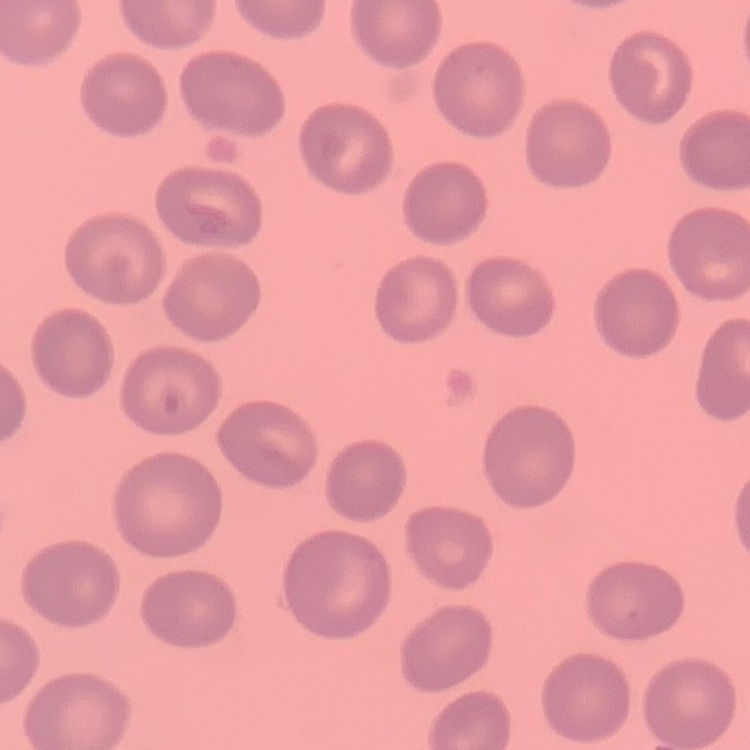 The erythrocytes show no rouleaux formation. Thin blood smear. Stained with either Field's or Giemsa. Square crop of a larger photomicrograph.